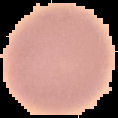

Summary:
  - Result: no Plasmodium parasites detected
  - Image size: 118×118 pixels
  - Image type: cell region segmented out of the field of view; surrounding area masked to black
  - Preparation: thin blood smear